Locate every leukocyte (white blood cell).
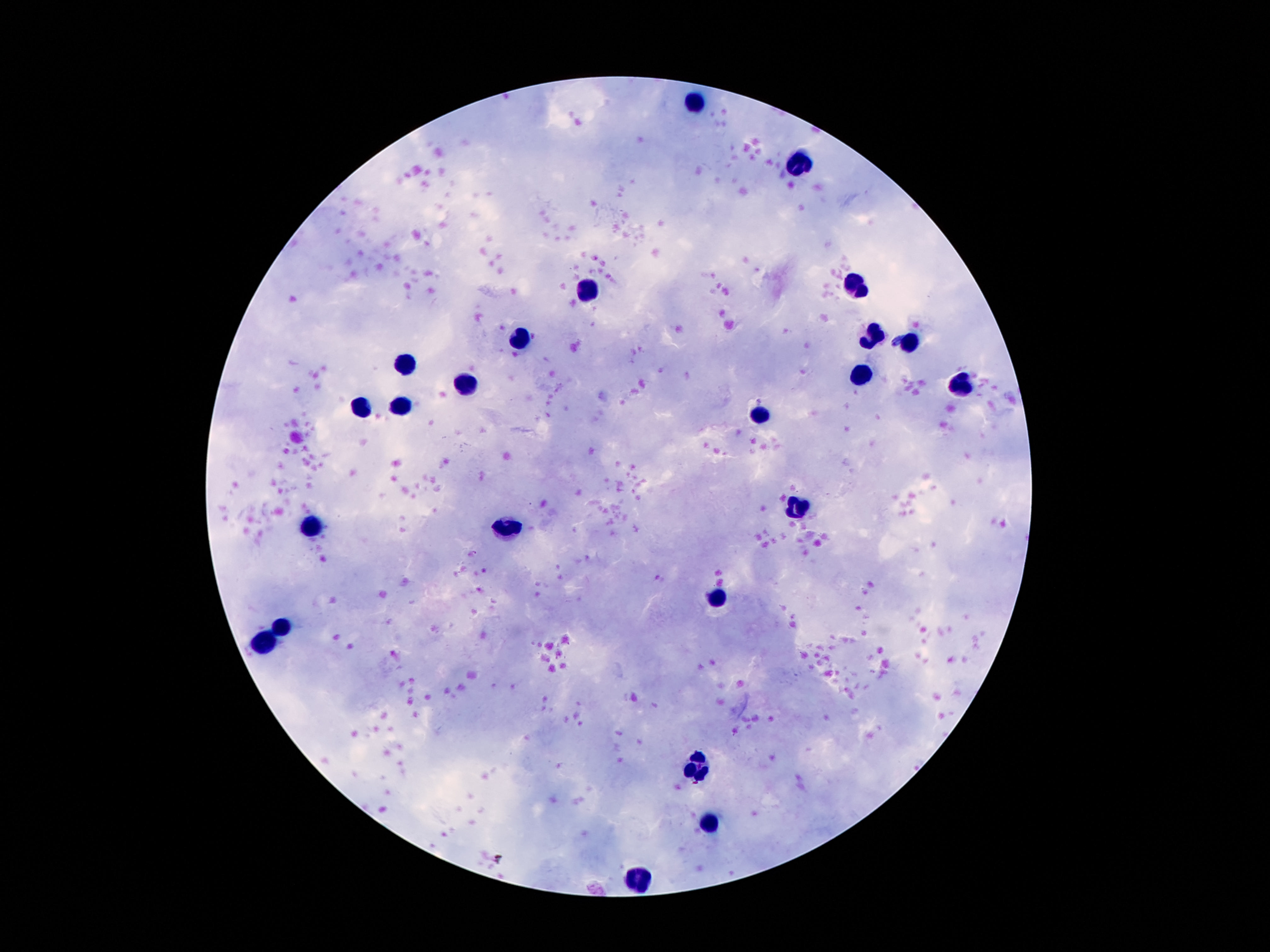
Approximate centers as [x, y] in pixels.
Leukocytes: [694, 105], [799, 168], [584, 285], [857, 285], [871, 334], [524, 337], [909, 345], [402, 364], [864, 376], [960, 386], [465, 388], [402, 404], [362, 406], [759, 416], [797, 508], [309, 527], [503, 528], [715, 598], [283, 624], [264, 640], [696, 767], [710, 819], [640, 878].

One field from this slide. Smartphone photograph taken through the microscope eyepiece. Image is 1270×952 pixels. Giemsa-stained preparation. 100x magnification. Thick blood smear. Patient malaria status: negative.